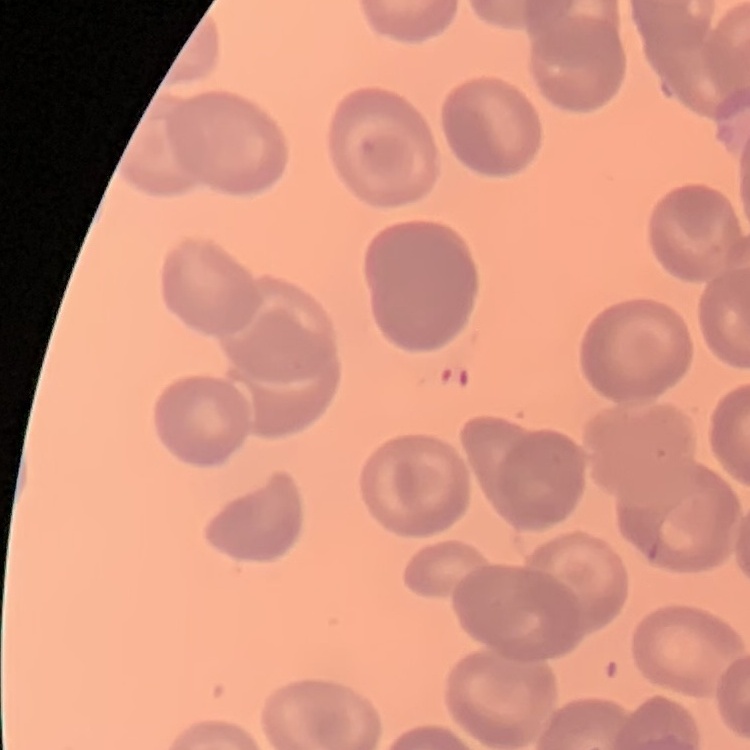

Summary:
  - Erythrocyte morphology: no rouleaux formation
  - Image type: square crop of a larger photomicrograph
  - Preparation: thin peripheral smear
  - Stain: Field's or Giemsa